Give the extent of all uninfected red blood cells.
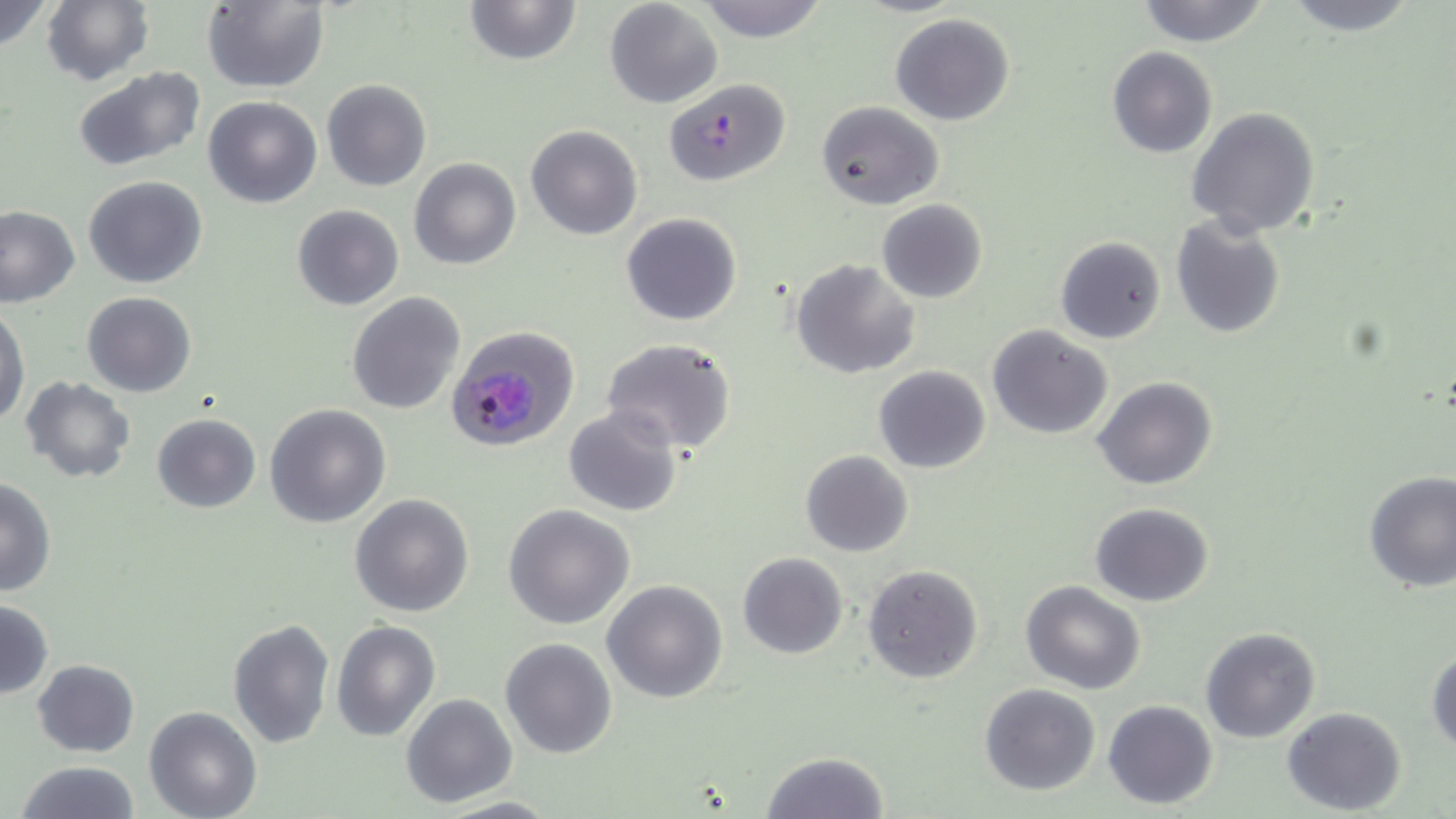

Approximate bounding boxes as (x1,y1)-(x2,y2) corner pairs in pixels.
Uninfected red blood cells: (0,0)-(55,52), (42,0)-(154,87), (463,0)-(582,66), (604,0)-(723,109), (695,0)-(829,40), (1134,0)-(1272,46), (1277,0)-(1425,36), (201,1)-(329,92), (890,14)-(1015,126), (1107,47)-(1217,159), (71,68)-(206,172), (321,79)-(431,191), (204,95)-(323,207), (816,102)-(944,211), (1187,106)-(1321,237), (526,125)-(642,240), (410,159)-(521,270), (83,176)-(209,289), (876,199)-(987,303), (292,204)-(405,311), (0,207)-(80,306), (620,212)-(743,326), (1170,215)-(1286,340), (1054,236)-(1167,345), (792,258)-(920,380), (82,291)-(197,397), (348,291)-(465,414), (0,303)-(30,425), (986,325)-(1113,440), (601,340)-(737,455), (873,365)-(991,474), (21,377)-(135,482), (1095,377)-(1218,490), (264,403)-(392,528), (563,406)-(683,516), (152,413)-(260,514), (800,450)-(915,557), (1363,470)-(1455,593), (0,478)-(56,595), (349,494)-(474,617), (1089,503)-(1212,606), (504,505)-(636,629), (737,552)-(849,659), (863,565)-(983,683), (602,579)-(727,702), (1021,581)-(1147,695), (0,598)-(53,701), (227,618)-(335,751), (332,620)-(440,741), (1199,627)-(1321,744), (500,637)-(617,758), (1428,648)-(1456,755), (31,658)-(141,757), (978,683)-(1101,796), (401,694)-(517,807), (1103,699)-(1218,808), (1282,706)-(1406,814), (144,707)-(264,819), (760,750)-(888,818), (15,760)-(140,818), (433,796)-(563,817).

Plasmodium falciparum-infected red blood cell locations: (661,77)-(791,187), (444,325)-(580,451). Slide-level diagnosis: Plasmodium falciparum. One field of a larger specimen. Optical microscopy. Captured at 1000x magnification. May-Grünwald-Giemsa-stained preparation. Thin blood smear. Image is 1456×819 pixels.